Evaluate for Plasmodium parasites.
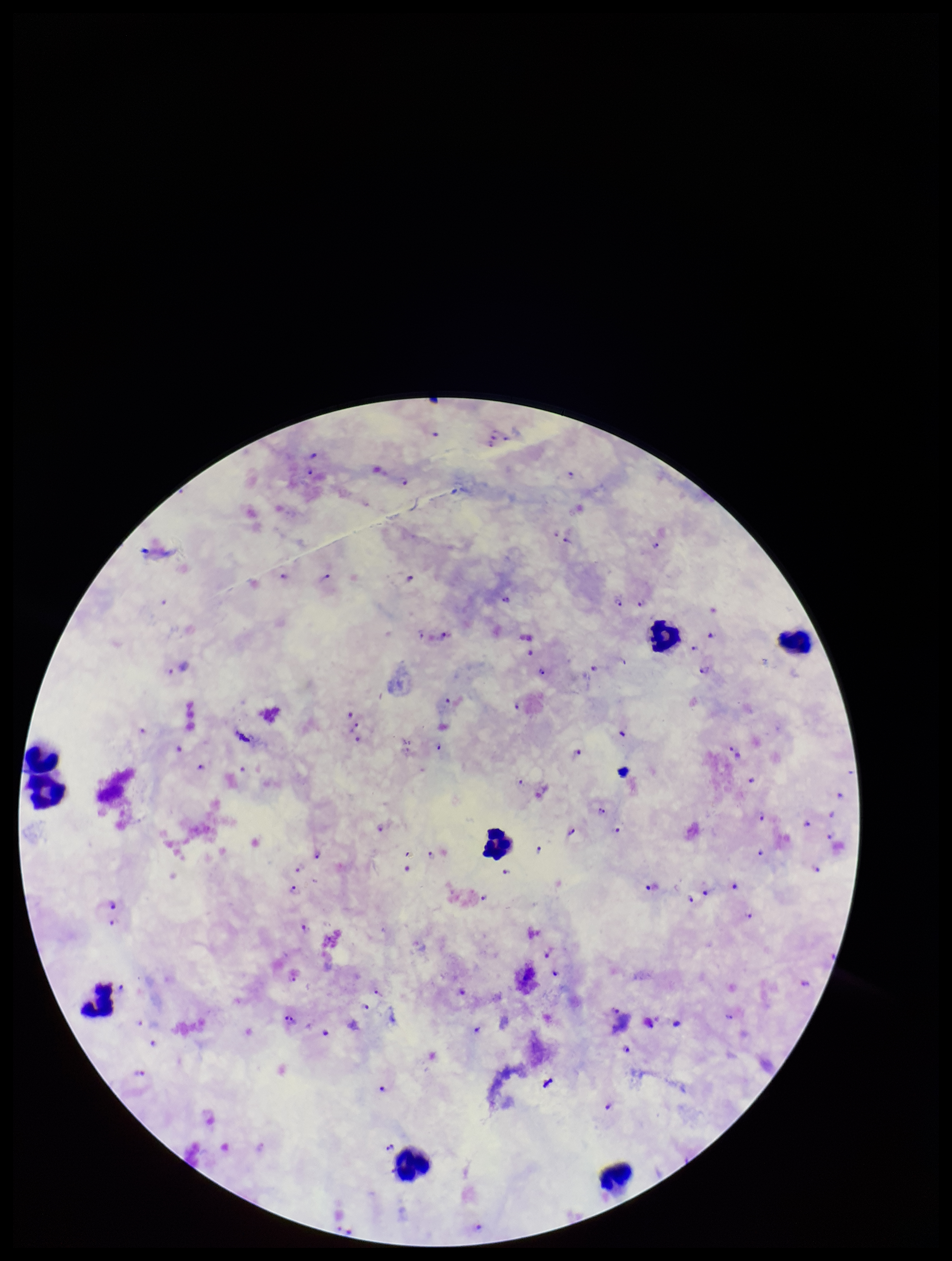

Seen.

Parasite count: 90. Species reported for this patient: Plasmodium falciparum. Leukocyte count: 8. Stained with Giemsa. Preparation: thick blood smear. Patient malaria status: infected. Smartphone photograph taken through the eyepiece of a microscope. Image is 952×1261 pixels. Single field of view.